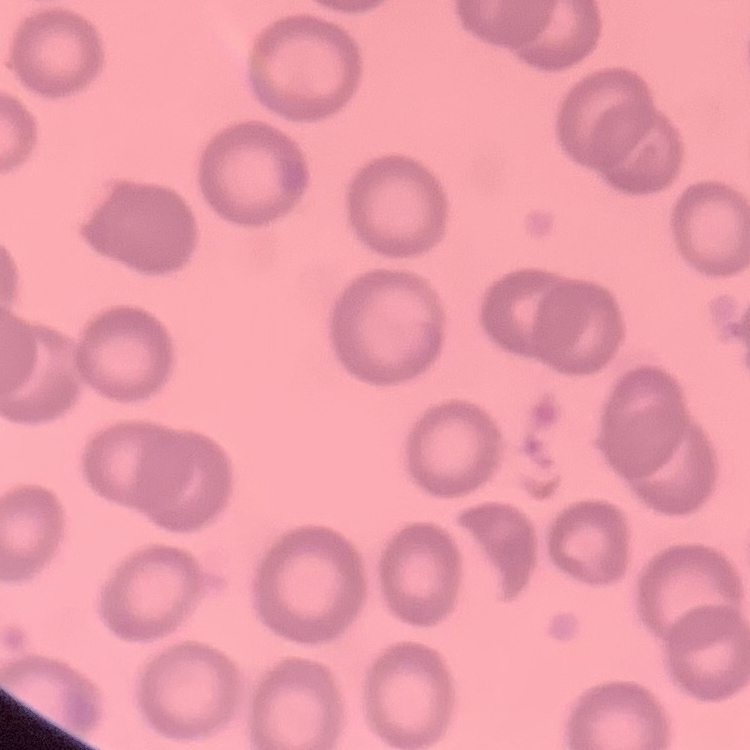

{
  "red_blood_cell_morphology": "no rouleaux formation",
  "image_type": "one tile cut from a larger photomicrograph",
  "stain": "Field's or Giemsa",
  "preparation": "thin peripheral smear"
}